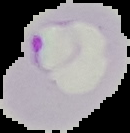
Summary:
  - Image size: 130×133 pixels
  - Preparation: thin blood film
  - Result: Plasmodium parasites identified
  - Image type: cell region segmented out of the field of view; surrounding area masked to black